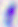

Summary:
  - Modality: micrograph
  - Magnification: 400x
  - Identification: Toxoplasma gondii